Name the parasite shown.
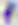
Toxoplasma gondii.

Photomicrograph. 400x magnification.